Assess this cell for malaria.
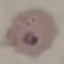

It is parasitized.

preparation = thin smear
capture = smartphone camera at the microscope eyepiece
image type = cell patch, automatically extracted from a larger field of view and resized to 64 × 64 pixels
stain = Giemsa